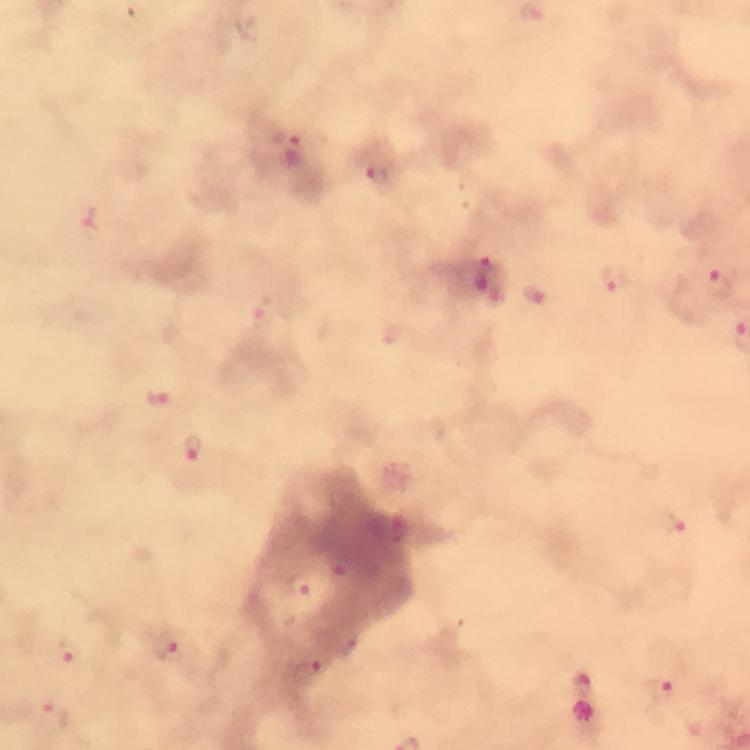
Approximate centers as (x, y) in pixels. Plasmodium parasite locations: (291, 154), (379, 182), (89, 217), (489, 280), (612, 283), (720, 284), (536, 297), (267, 315), (156, 400), (194, 450), (677, 533), (303, 585), (168, 648), (69, 653), (307, 674), (657, 692), (51, 714). Immersion oil applied. A crop from one field of view. 100x magnification. Photographed with a smartphone mounted on the microscope. Image is 750×750 pixels. From a diagnostic examination for malaria. Thick blood smear. Giemsa-stained preparation.